Outline each blood parasite and name the species.
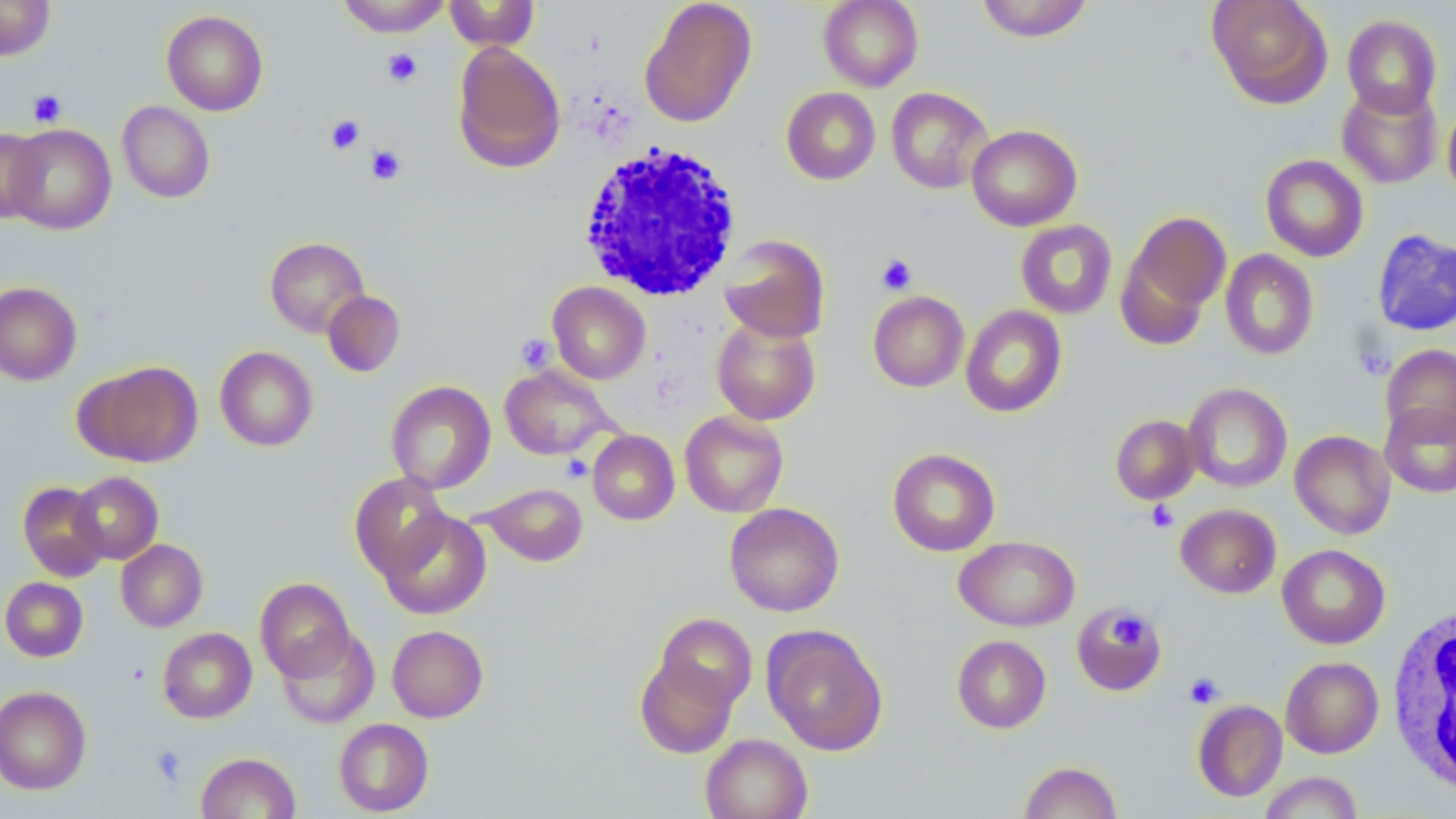
No blood parasites seen.

Approximate bounding boxes as [x1, y1, x2, y2] in pixels. White blood cell locations: [577, 141, 744, 302], [1386, 602, 1455, 796]. Platelet locations: [382, 48, 421, 86], [28, 90, 67, 126], [326, 115, 364, 154], [365, 144, 406, 185], [876, 253, 917, 295], [516, 334, 556, 373], [562, 456, 593, 482], [1147, 501, 1178, 532], [1108, 610, 1151, 648], [1184, 672, 1224, 708], [150, 744, 188, 785]. Uninfected red blood cell locations: [0, 0, 56, 61], [337, 0, 452, 37], [444, 0, 540, 51], [818, 0, 923, 91], [975, 0, 1094, 42], [1207, 0, 1333, 108], [639, 1, 757, 128], [161, 10, 268, 116], [1342, 14, 1442, 118], [452, 42, 566, 173], [1337, 83, 1442, 188], [781, 87, 881, 185], [886, 87, 993, 194], [1442, 100, 1456, 202], [118, 101, 215, 203], [5, 124, 116, 234], [966, 124, 1082, 231], [0, 128, 46, 224], [1260, 154, 1369, 262], [1118, 210, 1230, 339], [1015, 219, 1117, 319], [1372, 228, 1456, 337], [718, 235, 831, 343], [265, 236, 369, 337], [1220, 249, 1319, 360], [0, 281, 82, 385], [548, 282, 651, 384], [322, 290, 405, 377], [867, 290, 969, 392], [961, 305, 1067, 418], [711, 317, 821, 425], [1381, 343, 1456, 444], [215, 346, 318, 451], [77, 360, 203, 467], [500, 365, 616, 460], [386, 380, 496, 493], [1183, 383, 1292, 493], [1380, 401, 1456, 497], [679, 410, 789, 518], [1110, 414, 1200, 504], [587, 430, 680, 525], [1290, 430, 1396, 539], [888, 448, 1001, 556], [70, 471, 163, 564], [349, 473, 452, 579], [17, 481, 109, 581], [481, 482, 587, 567], [724, 502, 844, 617], [1175, 503, 1281, 598], [377, 507, 491, 619], [955, 536, 1080, 631], [116, 539, 208, 632], [1277, 543, 1390, 649], [0, 576, 88, 662], [255, 577, 355, 682], [1071, 603, 1166, 696], [655, 612, 757, 711], [386, 624, 488, 722], [764, 626, 887, 755], [158, 627, 257, 723], [275, 627, 380, 729], [951, 634, 1052, 733], [634, 654, 740, 759], [1281, 656, 1384, 758], [0, 686, 91, 795], [1192, 699, 1287, 801], [333, 718, 434, 816], [700, 733, 813, 819], [196, 752, 301, 818], [1019, 761, 1122, 819], [1258, 772, 1363, 818]. Slide-level diagnosis: negative for blood parasites. Image is 1456×819 pixels. Thin blood smear. Light microscopy. One field of a larger specimen. May-Grünwald-Giemsa-stained preparation. 1000x magnification.